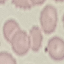 Malaria status: uninfected. Giemsa-stained preparation. Acquired by smartphone through the microscope eyepiece. Automatically extracted cell patch, resized to 64 × 64 pixels. Thin smear of blood.